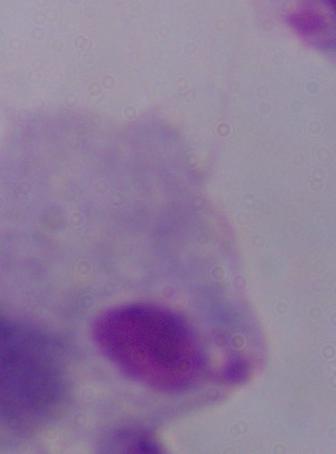
magnification = 1000x
identification = trichomonad
modality = photomicrograph